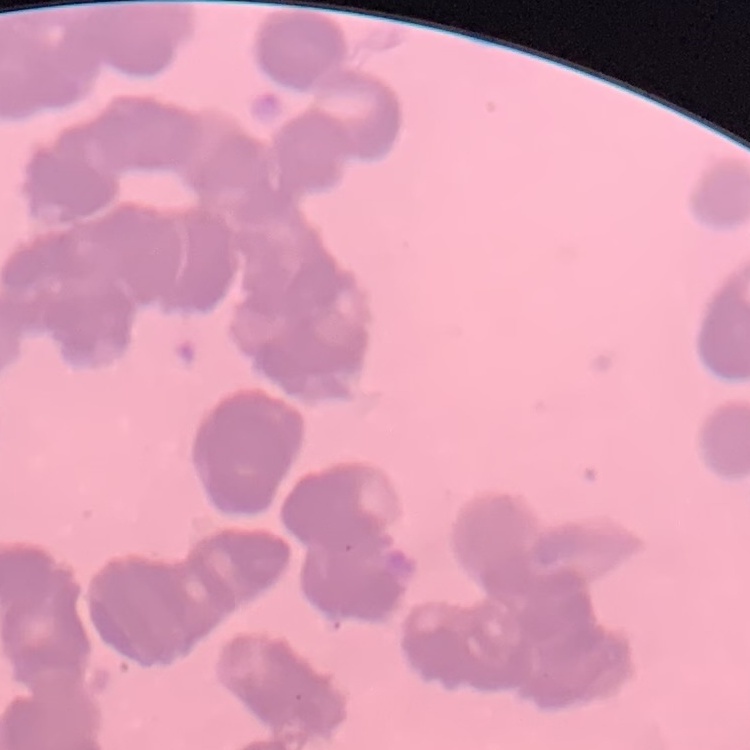
The erythrocytes show rouleaux formation. Thin peripheral smear. Square crop of a larger photomicrograph. Field's or Giemsa stain.